Outline each blood parasite and name the species.
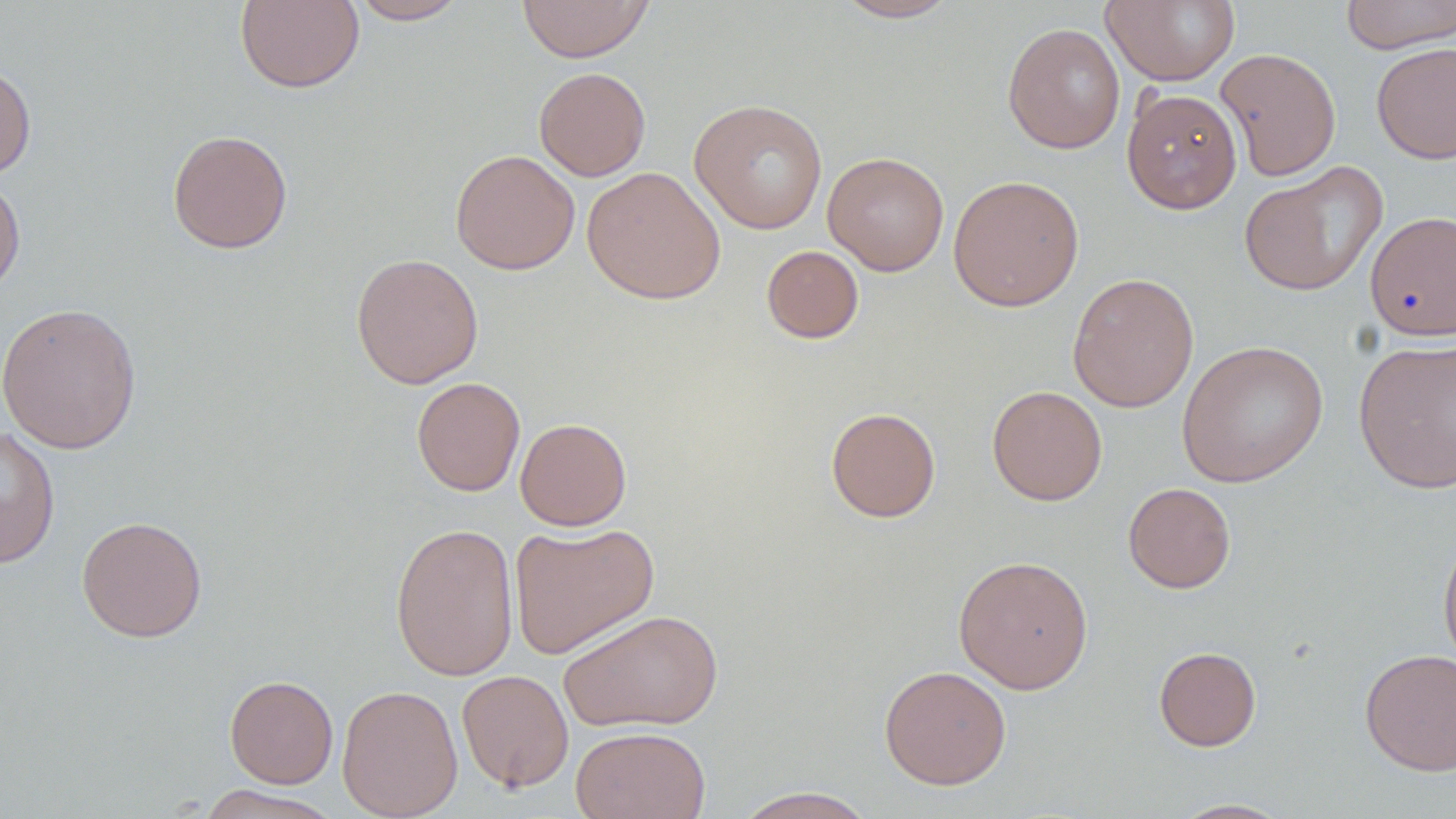

No blood parasites observed.

Approximate bounding boxes as (x1, y1, x2, y2) in pixels. Uninfected red blood cell locations: (516, 0, 654, 63), (828, 0, 966, 23), (1101, 0, 1241, 87), (1340, 0, 1455, 54), (235, 1, 364, 93), (347, 1, 470, 24), (1002, 22, 1125, 154), (1371, 42, 1456, 165), (1215, 48, 1342, 181), (0, 62, 36, 180), (534, 67, 651, 181), (1121, 88, 1242, 215), (689, 97, 829, 235), (167, 129, 293, 254), (450, 149, 580, 275), (822, 152, 950, 276), (1239, 162, 1387, 297), (582, 166, 726, 304), (0, 173, 26, 299), (948, 174, 1085, 312), (1364, 210, 1456, 341), (761, 245, 864, 344), (350, 252, 485, 389), (1067, 272, 1199, 413), (0, 302, 142, 455), (1353, 337, 1456, 494), (1176, 339, 1329, 488), (411, 377, 525, 496), (986, 385, 1107, 506), (825, 407, 941, 522), (515, 417, 632, 531), (1, 426, 60, 568), (1123, 482, 1235, 593), (77, 515, 207, 642), (390, 522, 519, 681), (508, 522, 660, 660), (1438, 527, 1456, 674), (953, 554, 1094, 694), (559, 608, 725, 733), (1154, 646, 1261, 751), (1359, 648, 1456, 777), (879, 665, 1012, 790), (457, 669, 574, 792), (224, 675, 338, 789), (337, 684, 463, 819), (570, 725, 710, 819), (195, 785, 345, 819), (731, 787, 879, 819), (1167, 798, 1296, 818). Slide-level diagnosis: no evidence of blood parasites. One field of a larger specimen. Image is 1456×819 pixels. Light microscopy. Thin blood smear. 1000x magnification. May-Grünwald-Giemsa-stained preparation.